Locate every P. falciparum parasite and identify its life-cycle stage.
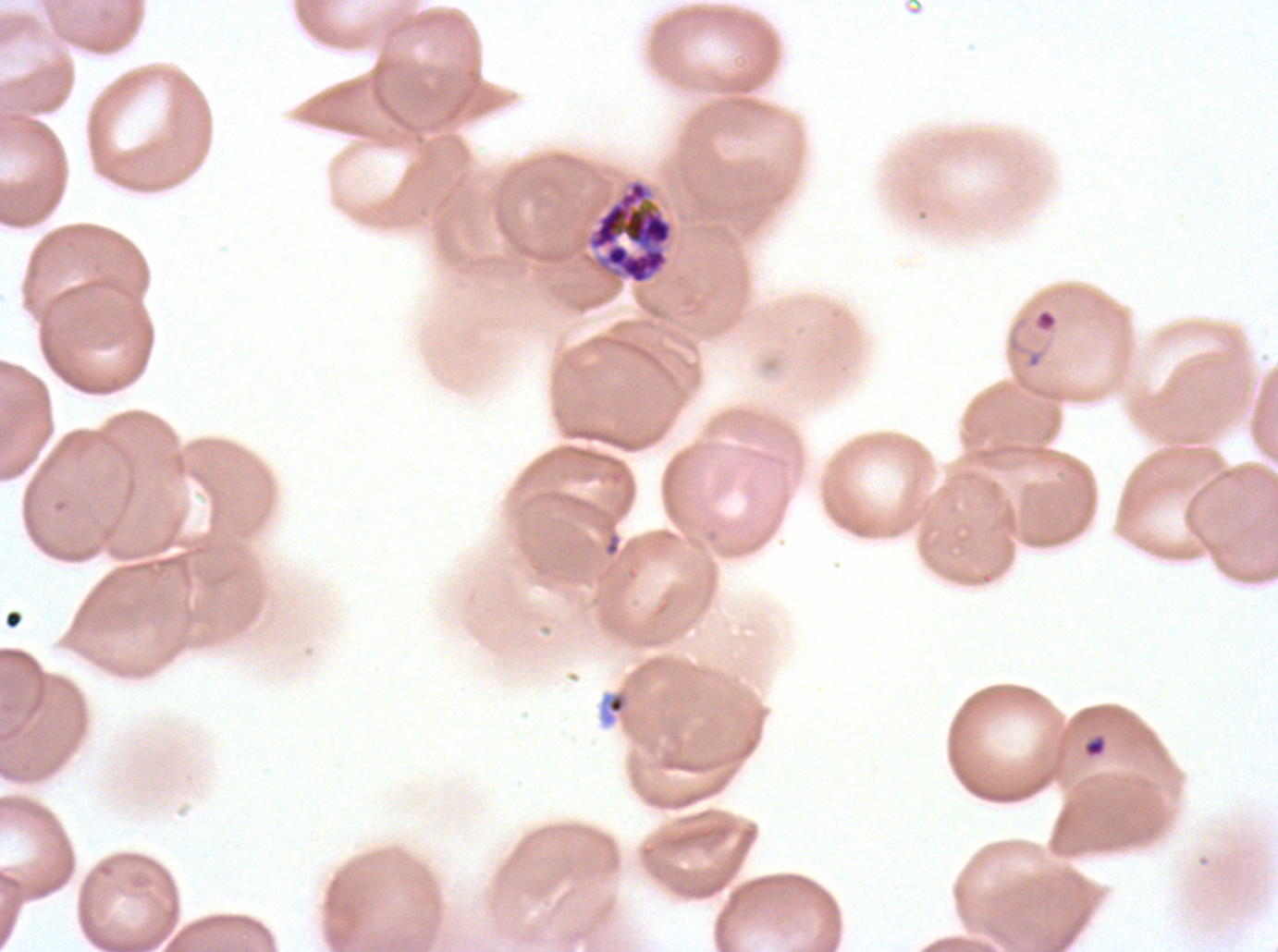
Approximate bounding boxes as (x1, y1, x2, y2) in pixels.
Rings: (1035, 309, 1057, 332).
Late schizonts: (584, 177, 675, 286).
No late-ring/early-trophozoite forms, mid trophozoites, late trophozoites, early schizonts, segmenters, or gametocytes observed.

Debris locations: (597, 688, 632, 728), (1082, 733, 1108, 759). Thin blood film. A sub-image separated from a larger composite. Life-cycle stages observed: ring, late schizont. Ex-vivo P. falciparum culture from a patient in The Gambia, grown for 24 to 48 hours. Giemsa stain. Image is 1278×952 pixels.